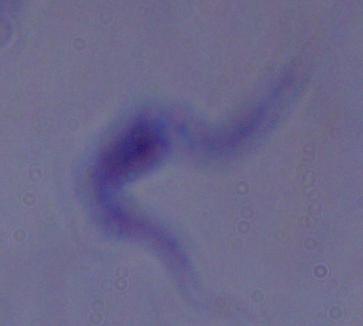

Summary:
  - Identification: trypanosome
  - Magnification: 1000x
  - Modality: micrograph